Comment on the morphology of the red blood cells.
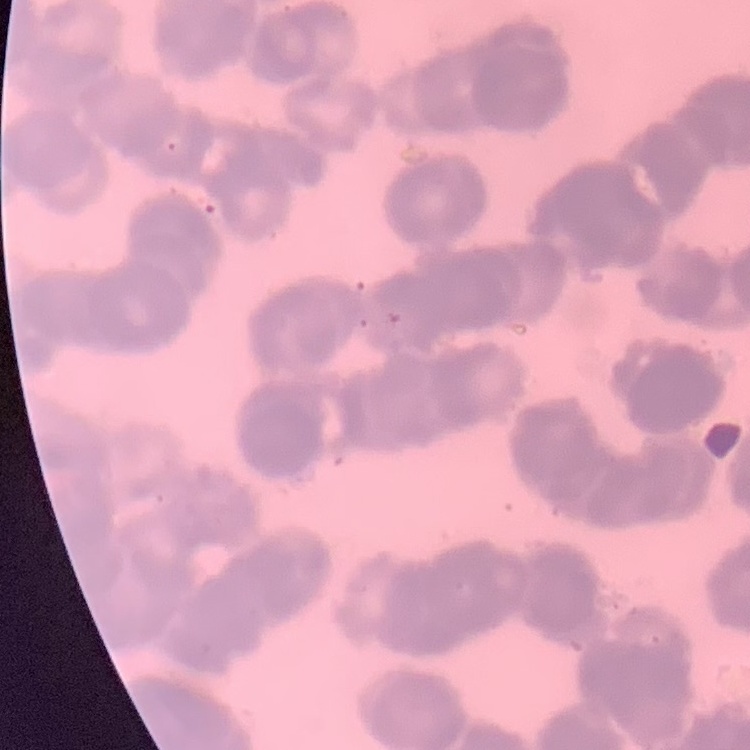

They show rouleaux formation.

Summary:
  - Image type: one tile cut from a larger photomicrograph
  - Preparation: thin blood film
  - Stain: Field's or Giemsa